Report the malaria status of this cell.
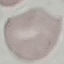
It is uninfected.

{
  "image_type": "automatically extracted cell patch, resized to 64 × 64 pixels",
  "stain": "Giemsa",
  "capture": "smartphone camera at the microscope eyepiece",
  "preparation": "thin blood film"
}